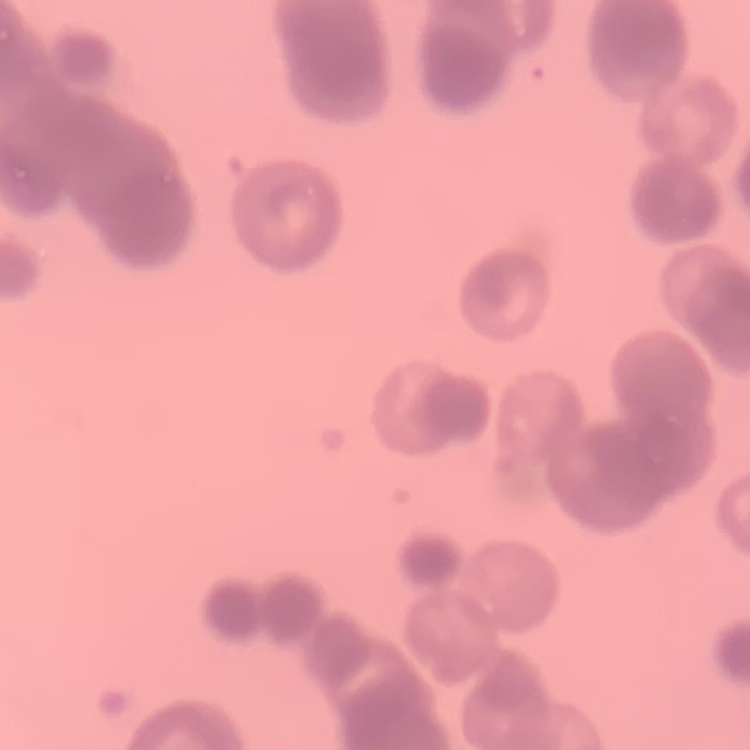
Summary:
  - Red blood cell morphology: rouleaux formation
  - Stain: Field's or Giemsa
  - Image type: square crop of a larger photomicrograph
  - Preparation: thin blood smear